Report the malaria status of this cell.
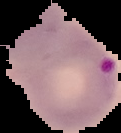

Parasitized.

Cell region segmented out of the field of view; the surrounding area is masked to black. From a thin blood film. Image is 121×133 pixels.